Locate the red blood cells and classify each one as Plasmodium falciparum-infected, uninfected, or of indeterminate infection status.
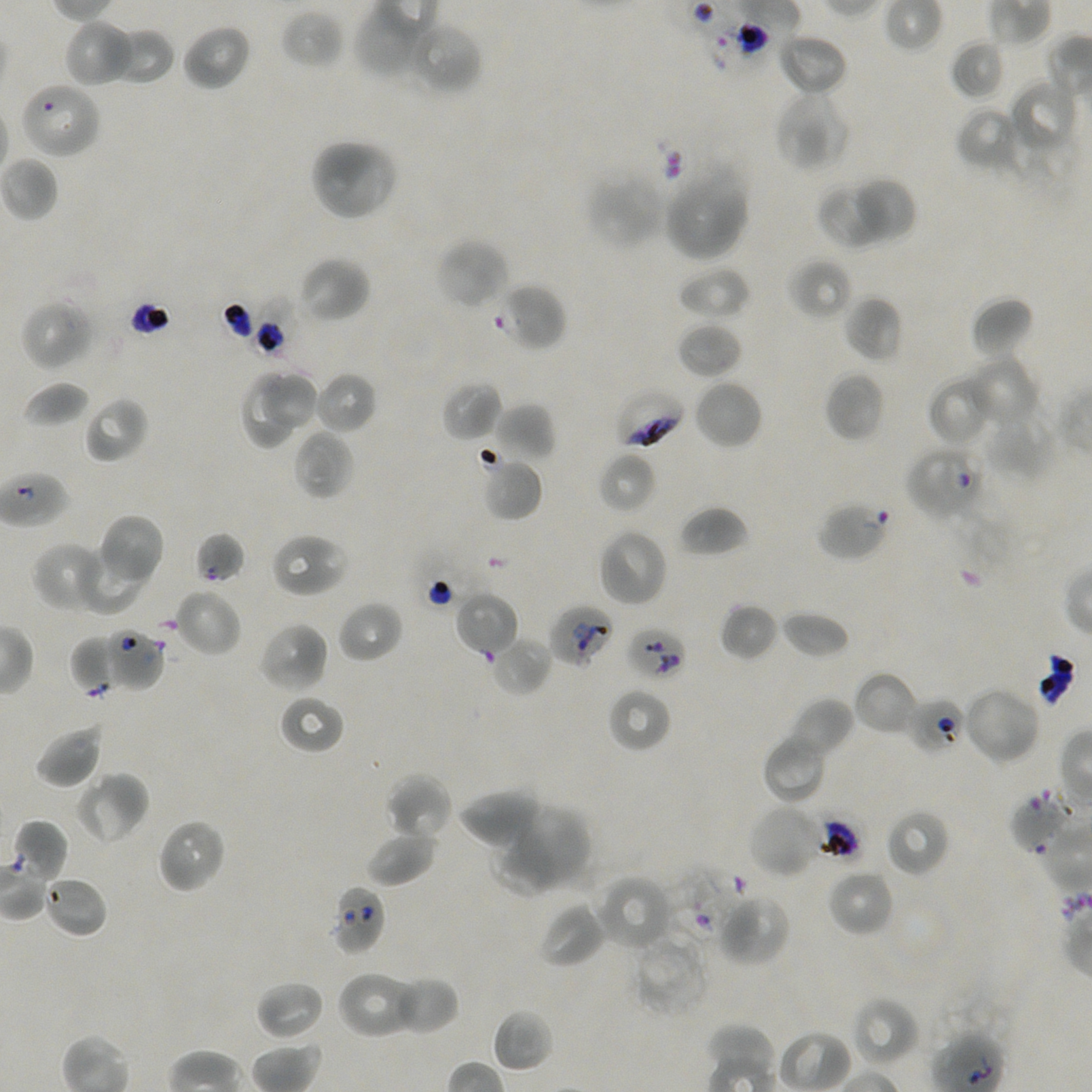

Approximate bounding rectangles given as corner coordinates in pixels from the top-left. Not every red blood cell is marked.
Infected red blood cells: (x1=613, y1=388, x2=685, y2=450).
Red blood cells of indeterminate infection status: (x1=19, y1=80, x2=103, y2=160), (x1=497, y1=283, x2=567, y2=352), (x1=253, y1=297, x2=310, y2=361), (x1=905, y1=445, x2=986, y2=521), (x1=194, y1=531, x2=246, y2=584), (x1=549, y1=604, x2=615, y2=668), (x1=627, y1=625, x2=687, y2=682), (x1=101, y1=628, x2=165, y2=692), (x1=908, y1=697, x2=966, y2=755), (x1=1008, y1=788, x2=1078, y2=854), (x1=12, y1=818, x2=69, y2=884), (x1=666, y1=867, x2=746, y2=945), (x1=330, y1=884, x2=386, y2=956).
Uninfected red blood cells: (x1=354, y1=2, x2=429, y2=79), (x1=280, y1=9, x2=345, y2=70), (x1=65, y1=19, x2=137, y2=88), (x1=405, y1=20, x2=484, y2=96), (x1=181, y1=23, x2=251, y2=92), (x1=106, y1=26, x2=175, y2=86), (x1=777, y1=33, x2=848, y2=97), (x1=949, y1=39, x2=1006, y2=101), (x1=1007, y1=79, x2=1078, y2=156), (x1=775, y1=89, x2=851, y2=172), (x1=956, y1=105, x2=1027, y2=175), (x1=309, y1=137, x2=399, y2=221), (x1=663, y1=166, x2=750, y2=262), (x1=585, y1=171, x2=666, y2=250), (x1=858, y1=176, x2=916, y2=242), (x1=816, y1=182, x2=888, y2=250), (x1=435, y1=237, x2=511, y2=310), (x1=299, y1=256, x2=370, y2=323), (x1=789, y1=257, x2=854, y2=321), (x1=676, y1=266, x2=750, y2=320), (x1=843, y1=295, x2=903, y2=363), (x1=970, y1=295, x2=1034, y2=360), (x1=21, y1=298, x2=96, y2=372), (x1=676, y1=321, x2=742, y2=379), (x1=964, y1=354, x2=1040, y2=430), (x1=240, y1=370, x2=297, y2=450), (x1=314, y1=371, x2=378, y2=435), (x1=824, y1=371, x2=886, y2=442), (x1=260, y1=373, x2=323, y2=431), (x1=926, y1=375, x2=994, y2=447), (x1=694, y1=379, x2=763, y2=450), (x1=22, y1=380, x2=91, y2=428), (x1=441, y1=380, x2=502, y2=443), (x1=84, y1=396, x2=149, y2=464), (x1=492, y1=402, x2=556, y2=463), (x1=983, y1=407, x2=1056, y2=481), (x1=293, y1=428, x2=354, y2=500), (x1=598, y1=451, x2=657, y2=514), (x1=479, y1=456, x2=543, y2=522), (x1=816, y1=502, x2=890, y2=562), (x1=678, y1=505, x2=748, y2=558), (x1=98, y1=513, x2=165, y2=587), (x1=597, y1=528, x2=668, y2=608), (x1=270, y1=532, x2=349, y2=598), (x1=31, y1=541, x2=111, y2=614), (x1=78, y1=542, x2=145, y2=615), (x1=175, y1=588, x2=242, y2=657), (x1=454, y1=590, x2=519, y2=659), (x1=337, y1=600, x2=403, y2=663), (x1=719, y1=602, x2=779, y2=661), (x1=782, y1=610, x2=850, y2=659), (x1=258, y1=621, x2=329, y2=693), (x1=69, y1=634, x2=125, y2=695), (x1=490, y1=634, x2=552, y2=697), (x1=853, y1=671, x2=920, y2=736), (x1=961, y1=685, x2=1042, y2=767), (x1=606, y1=687, x2=672, y2=754), (x1=278, y1=695, x2=345, y2=756), (x1=788, y1=697, x2=855, y2=757), (x1=34, y1=723, x2=104, y2=789), (x1=763, y1=733, x2=829, y2=803), (x1=74, y1=769, x2=150, y2=845), (x1=384, y1=773, x2=453, y2=840), (x1=458, y1=788, x2=543, y2=849), (x1=509, y1=803, x2=592, y2=881), (x1=747, y1=803, x2=825, y2=879), (x1=885, y1=809, x2=950, y2=878), (x1=156, y1=818, x2=226, y2=895), (x1=365, y1=827, x2=437, y2=887), (x1=489, y1=830, x2=562, y2=898), (x1=828, y1=869, x2=895, y2=937), (x1=594, y1=873, x2=674, y2=952), (x1=43, y1=875, x2=108, y2=939), (x1=715, y1=892, x2=792, y2=968), (x1=536, y1=900, x2=606, y2=968), (x1=632, y1=934, x2=710, y2=1017), (x1=336, y1=970, x2=419, y2=1040), (x1=396, y1=978, x2=459, y2=1034), (x1=255, y1=980, x2=325, y2=1041), (x1=852, y1=996, x2=920, y2=1068), (x1=491, y1=1008, x2=553, y2=1072).

objective = 100x, oil immersion, numerical aperture 1.45
field of view = single
preparation = thin blood film
image size = 1092×1092 pixels
donor blood group = A+/O+
culture = in-vitro Plasmodium falciparum strain NF54, static
stain = Giemsa